Assess the morphology of the erythrocytes.
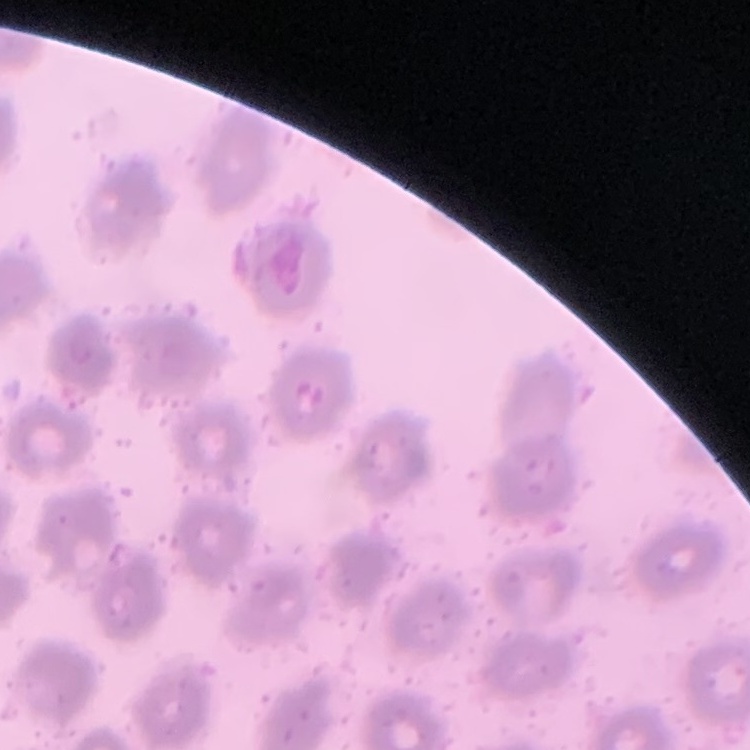
No rouleaux formation.

preparation = thin blood film
image type = one tile cut from a larger photomicrograph
stain = Field's or Giemsa